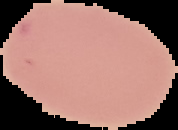

Summary:
  - Preparation: thin blood smear
  - Result: no Plasmodium parasites detected
  - Image size: 178×130 pixels
  - Image type: cell region segmented out of the field of view; surrounding area masked to black